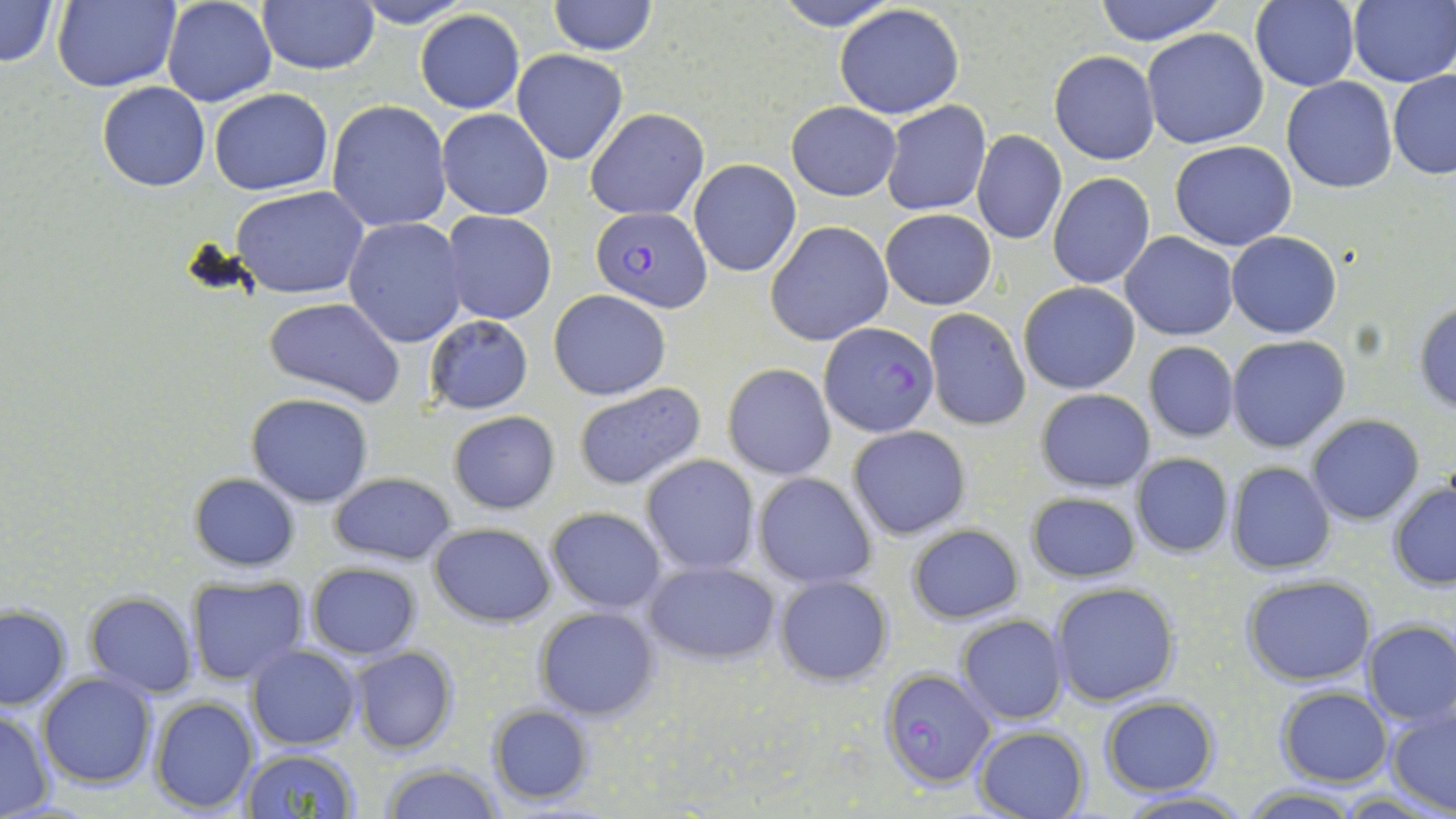
slide-level diagnosis = Plasmodium falciparum
stain = May-Grünwald-Giemsa
Plasmodium falciparum-infected red blood cell locations = approximate bounding boxes as named x1/y1/x2/y2 corners in pixels: (x1=591, y1=207, x2=711, y2=310), (x1=821, y1=323, x2=940, y2=438), (x1=880, y1=667, x2=995, y2=789)
uninfected red blood cell locations = approximate bounding boxes as named x1/y1/x2/y2 corners in pixels: (x1=0, y1=0, x2=60, y2=68), (x1=54, y1=0, x2=181, y2=93), (x1=161, y1=0, x2=277, y2=108), (x1=257, y1=0, x2=380, y2=76), (x1=348, y1=0, x2=474, y2=28), (x1=547, y1=0, x2=657, y2=55), (x1=771, y1=0, x2=904, y2=30), (x1=1089, y1=0, x2=1227, y2=45), (x1=1250, y1=0, x2=1361, y2=91), (x1=1348, y1=1, x2=1456, y2=87), (x1=834, y1=4, x2=965, y2=118), (x1=415, y1=9, x2=524, y2=114), (x1=1142, y1=28, x2=1269, y2=148), (x1=512, y1=49, x2=628, y2=165), (x1=1049, y1=50, x2=1159, y2=165), (x1=1388, y1=69, x2=1456, y2=179), (x1=1282, y1=76, x2=1398, y2=192), (x1=97, y1=81, x2=210, y2=191), (x1=209, y1=88, x2=333, y2=195), (x1=328, y1=99, x2=451, y2=232), (x1=883, y1=102, x2=991, y2=215), (x1=787, y1=103, x2=901, y2=201), (x1=436, y1=108, x2=553, y2=220), (x1=585, y1=108, x2=709, y2=220), (x1=973, y1=130, x2=1067, y2=245), (x1=1170, y1=140, x2=1297, y2=250), (x1=688, y1=159, x2=802, y2=276), (x1=1047, y1=173, x2=1154, y2=288), (x1=231, y1=187, x2=370, y2=297), (x1=880, y1=209, x2=996, y2=310), (x1=441, y1=211, x2=557, y2=325), (x1=343, y1=218, x2=468, y2=347), (x1=765, y1=220, x2=895, y2=345), (x1=1121, y1=231, x2=1238, y2=341), (x1=1226, y1=231, x2=1342, y2=338), (x1=1017, y1=281, x2=1141, y2=394), (x1=548, y1=288, x2=672, y2=401), (x1=264, y1=296, x2=408, y2=405), (x1=1412, y1=299, x2=1456, y2=413), (x1=923, y1=308, x2=1031, y2=430), (x1=424, y1=314, x2=534, y2=414), (x1=1226, y1=335, x2=1351, y2=452), (x1=1142, y1=341, x2=1240, y2=443), (x1=723, y1=363, x2=836, y2=480), (x1=573, y1=383, x2=707, y2=491), (x1=1036, y1=388, x2=1155, y2=492), (x1=247, y1=392, x2=374, y2=506), (x1=448, y1=411, x2=561, y2=513), (x1=1307, y1=415, x2=1426, y2=525), (x1=847, y1=426, x2=970, y2=539), (x1=1131, y1=453, x2=1233, y2=558), (x1=640, y1=454, x2=760, y2=575), (x1=1226, y1=462, x2=1335, y2=575), (x1=752, y1=471, x2=877, y2=589), (x1=188, y1=472, x2=301, y2=573), (x1=329, y1=472, x2=455, y2=563), (x1=1388, y1=482, x2=1456, y2=591), (x1=1025, y1=490, x2=1141, y2=585), (x1=545, y1=506, x2=667, y2=612), (x1=429, y1=521, x2=556, y2=628), (x1=907, y1=523, x2=1024, y2=624), (x1=643, y1=559, x2=779, y2=665), (x1=306, y1=562, x2=421, y2=660), (x1=772, y1=575, x2=894, y2=685), (x1=1242, y1=575, x2=1377, y2=685), (x1=187, y1=577, x2=309, y2=684), (x1=1051, y1=582, x2=1179, y2=706), (x1=84, y1=592, x2=198, y2=696), (x1=0, y1=605, x2=72, y2=712), (x1=534, y1=606, x2=660, y2=720), (x1=956, y1=614, x2=1067, y2=725), (x1=1362, y1=619, x2=1456, y2=726), (x1=245, y1=645, x2=361, y2=749), (x1=351, y1=646, x2=460, y2=754), (x1=36, y1=673, x2=157, y2=788), (x1=1277, y1=687, x2=1391, y2=786), (x1=148, y1=696, x2=259, y2=816), (x1=1100, y1=696, x2=1219, y2=796), (x1=485, y1=703, x2=595, y2=806), (x1=1387, y1=705, x2=1456, y2=814), (x1=0, y1=707, x2=54, y2=817), (x1=973, y1=726, x2=1090, y2=818), (x1=241, y1=747, x2=361, y2=819), (x1=381, y1=763, x2=505, y2=819), (x1=1242, y1=786, x2=1361, y2=817), (x1=1114, y1=790, x2=1252, y2=818)
field of view = single
preparation = thin blood smear
magnification = 1000x
modality = light microscopy
image size = 1456×819 pixels